Report the malaria status of this cell.
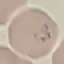

It is parasitized.

Photographed with a smartphone camera at the microscope eyepiece. Automatically extracted cell patch, resized to 64 × 64 pixels. Giemsa stain. Thin blood film.